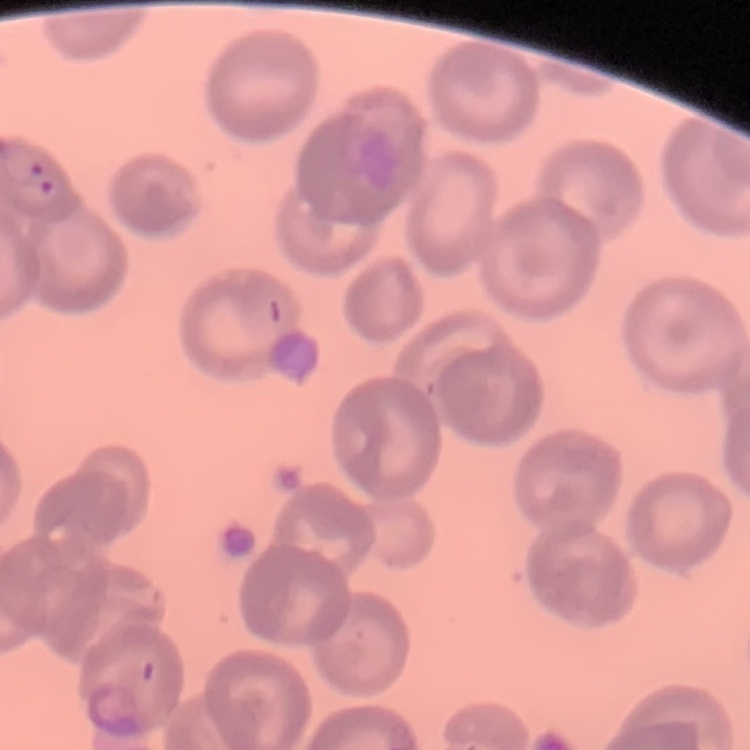

The erythrocytes show no rouleaux formation. Thin blood smear. Field's or Giemsa stain. Square crop of a larger photomicrograph.